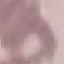
Summary:
  - Malaria status: uninfected
  - Capture: smartphone camera at the microscope eyepiece
  - Image type: cell patch, automatically extracted from a larger field of view and resized to 64 × 64 pixels
  - Stain: Giemsa
  - Preparation: thin blood smear